Describe the morphology of the red blood cells.
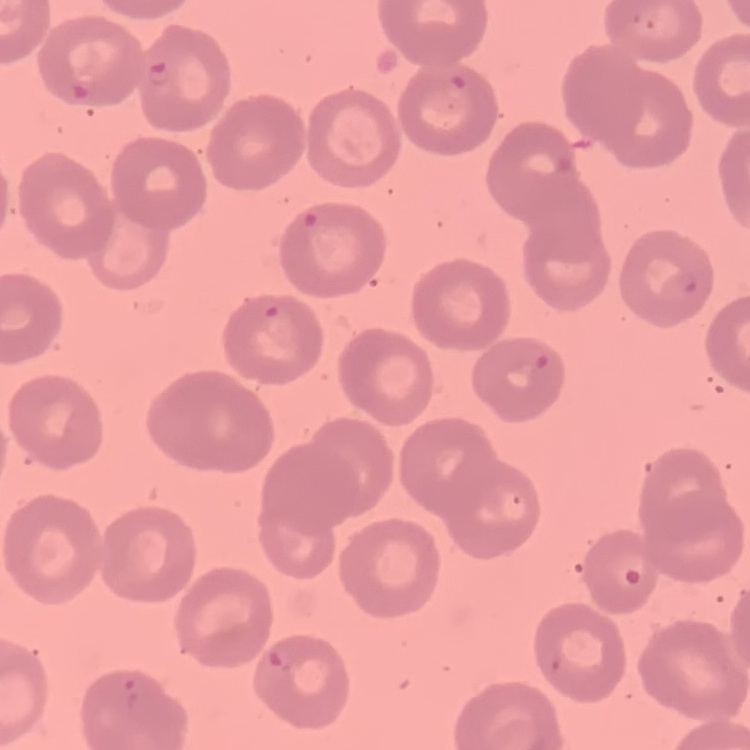

No rouleaux formation.

image_type: square crop of a larger photomicrograph
preparation: thin blood smear
stain: Field's or Giemsa